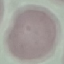

Summary:
  - Malaria status: uninfected
  - Preparation: thin blood film
  - Image type: automatically extracted cell patch, resized to 64 × 64 pixels
  - Capture: smartphone through the microscope eyepiece
  - Stain: Giemsa